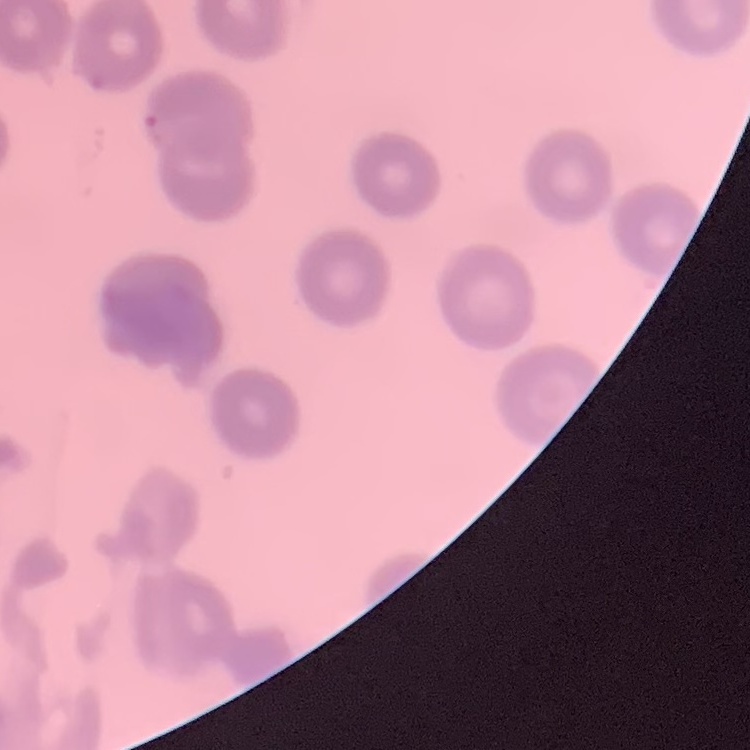
Summary:
  - Erythrocyte morphology: no rouleaux formation
  - Stain: Field's or Giemsa
  - Preparation: thin peripheral smear
  - Image type: square crop of a larger photomicrograph